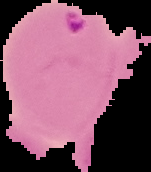
Summary:
  - Result: malaria parasites detected
  - Image size: 151×172 pixels
  - Preparation: thin blood smear
  - Image type: cell region segmented out of the field of view; surrounding area masked to black